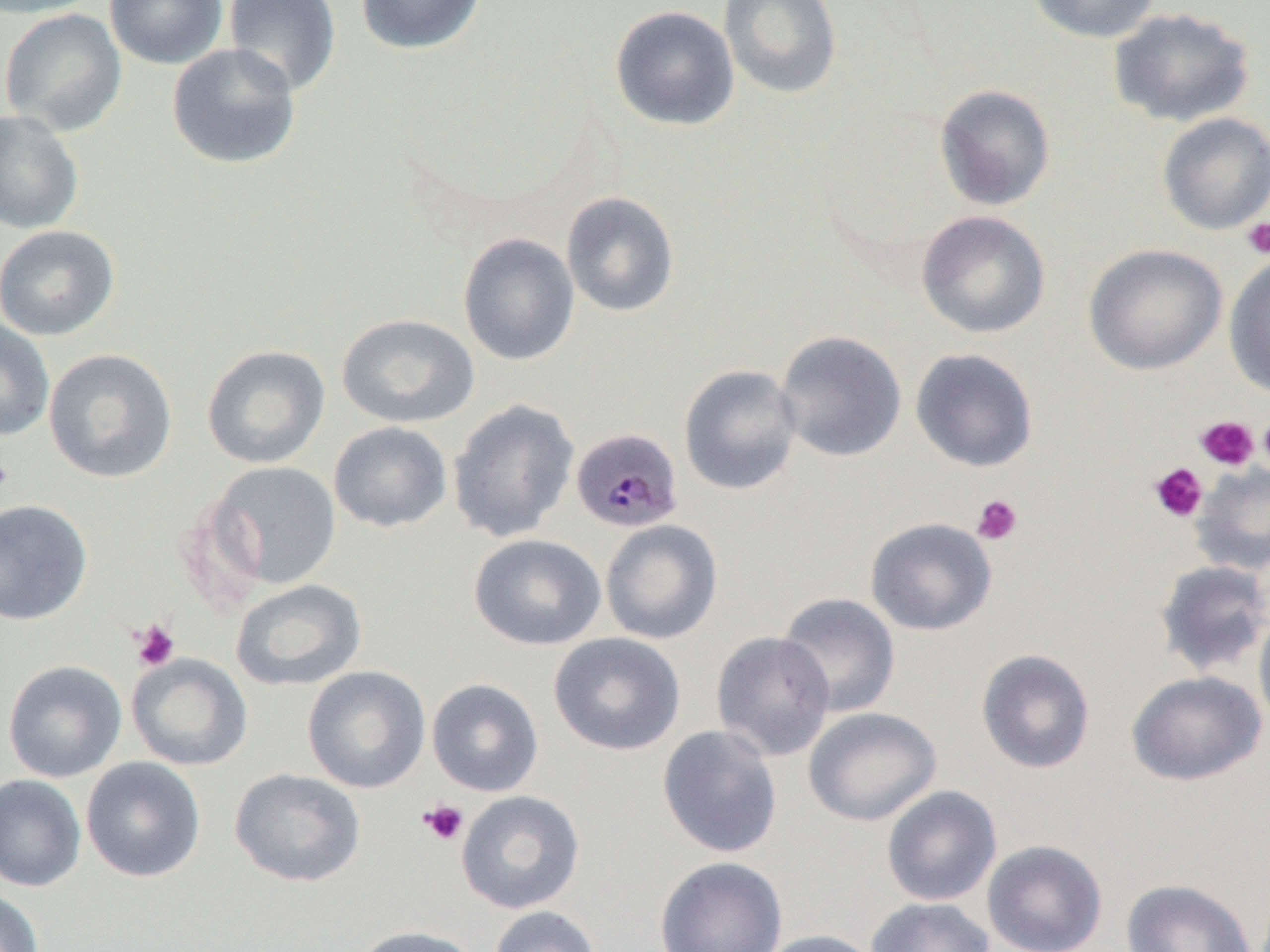 Approximate bounding boxes as named x1/y1/x2/y2 corners in pixels. Platelet locations: (x1=1240, y1=217, x2=1270, y2=260), (x1=1258, y1=411, x2=1270, y2=479), (x1=1195, y1=415, x2=1260, y2=471), (x1=0, y1=455, x2=13, y2=494), (x1=1148, y1=462, x2=1208, y2=522), (x1=971, y1=494, x2=1023, y2=546), (x1=130, y1=619, x2=180, y2=672), (x1=419, y1=799, x2=469, y2=845). Plasmodium malariae-infected red blood cell locations: (x1=575, y1=429, x2=687, y2=533). Uninfected red blood cell locations: (x1=0, y1=0, x2=103, y2=18), (x1=104, y1=0, x2=228, y2=69), (x1=223, y1=0, x2=341, y2=97), (x1=355, y1=0, x2=487, y2=55), (x1=719, y1=0, x2=842, y2=100), (x1=1026, y1=0, x2=1163, y2=44), (x1=610, y1=5, x2=740, y2=131), (x1=1108, y1=6, x2=1256, y2=128), (x1=0, y1=9, x2=127, y2=136), (x1=166, y1=42, x2=301, y2=169), (x1=933, y1=84, x2=1056, y2=211), (x1=0, y1=109, x2=84, y2=235), (x1=1157, y1=112, x2=1270, y2=235), (x1=561, y1=191, x2=679, y2=317), (x1=916, y1=210, x2=1051, y2=339), (x1=0, y1=225, x2=120, y2=340), (x1=458, y1=232, x2=580, y2=366), (x1=1083, y1=244, x2=1227, y2=375), (x1=1223, y1=253, x2=1270, y2=398), (x1=336, y1=313, x2=480, y2=429), (x1=0, y1=318, x2=55, y2=442), (x1=774, y1=330, x2=907, y2=462), (x1=201, y1=345, x2=331, y2=469), (x1=43, y1=348, x2=178, y2=484), (x1=909, y1=348, x2=1039, y2=472), (x1=678, y1=364, x2=803, y2=495), (x1=447, y1=399, x2=580, y2=543), (x1=329, y1=421, x2=452, y2=533), (x1=204, y1=461, x2=342, y2=591), (x1=1192, y1=462, x2=1270, y2=575), (x1=0, y1=498, x2=93, y2=626), (x1=865, y1=517, x2=997, y2=636), (x1=600, y1=519, x2=723, y2=644), (x1=468, y1=533, x2=606, y2=650), (x1=1154, y1=559, x2=1270, y2=678), (x1=230, y1=579, x2=367, y2=692), (x1=775, y1=592, x2=901, y2=718), (x1=1254, y1=608, x2=1270, y2=735), (x1=711, y1=631, x2=836, y2=761), (x1=548, y1=632, x2=686, y2=756), (x1=975, y1=648, x2=1096, y2=774), (x1=126, y1=653, x2=253, y2=771), (x1=3, y1=660, x2=127, y2=782), (x1=302, y1=665, x2=430, y2=793), (x1=1126, y1=670, x2=1267, y2=786), (x1=426, y1=678, x2=544, y2=797), (x1=803, y1=707, x2=941, y2=826), (x1=657, y1=724, x2=782, y2=858), (x1=81, y1=757, x2=205, y2=882), (x1=229, y1=768, x2=365, y2=887), (x1=0, y1=774, x2=86, y2=892), (x1=881, y1=785, x2=1002, y2=906), (x1=456, y1=790, x2=585, y2=914), (x1=982, y1=839, x2=1108, y2=952), (x1=654, y1=856, x2=788, y2=952), (x1=1121, y1=878, x2=1257, y2=952), (x1=0, y1=887, x2=45, y2=952), (x1=865, y1=896, x2=996, y2=952), (x1=487, y1=905, x2=602, y2=952), (x1=354, y1=925, x2=482, y2=952), (x1=756, y1=929, x2=885, y2=952). Slide-level diagnosis: Plasmodium malariae. 1000x magnification. Single field of view. Light microscopy. Image is 1270×952 pixels. Thin blood smear.